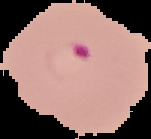
preparation = thin blood film
malaria status = parasitized
image type = segmented cell region with the area outside set to black
image size = 151×139 pixels